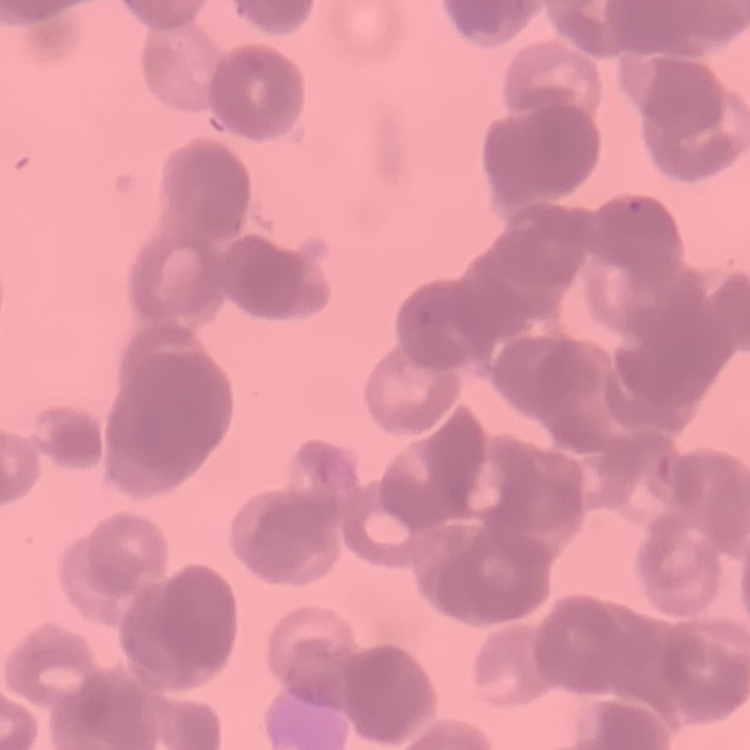
The red blood cells show rouleaux formation. Square crop of a larger photomicrograph. Stained with either Field's or Giemsa. Thin blood film.